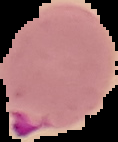 Image is 118×142 pixels. From a thin blood smear. Cell region segmented out of the field of view; the surrounding area is masked to black. Result: malaria parasites identified.